Give the extent of all Plasmodium falciparum-infected red blood cells.
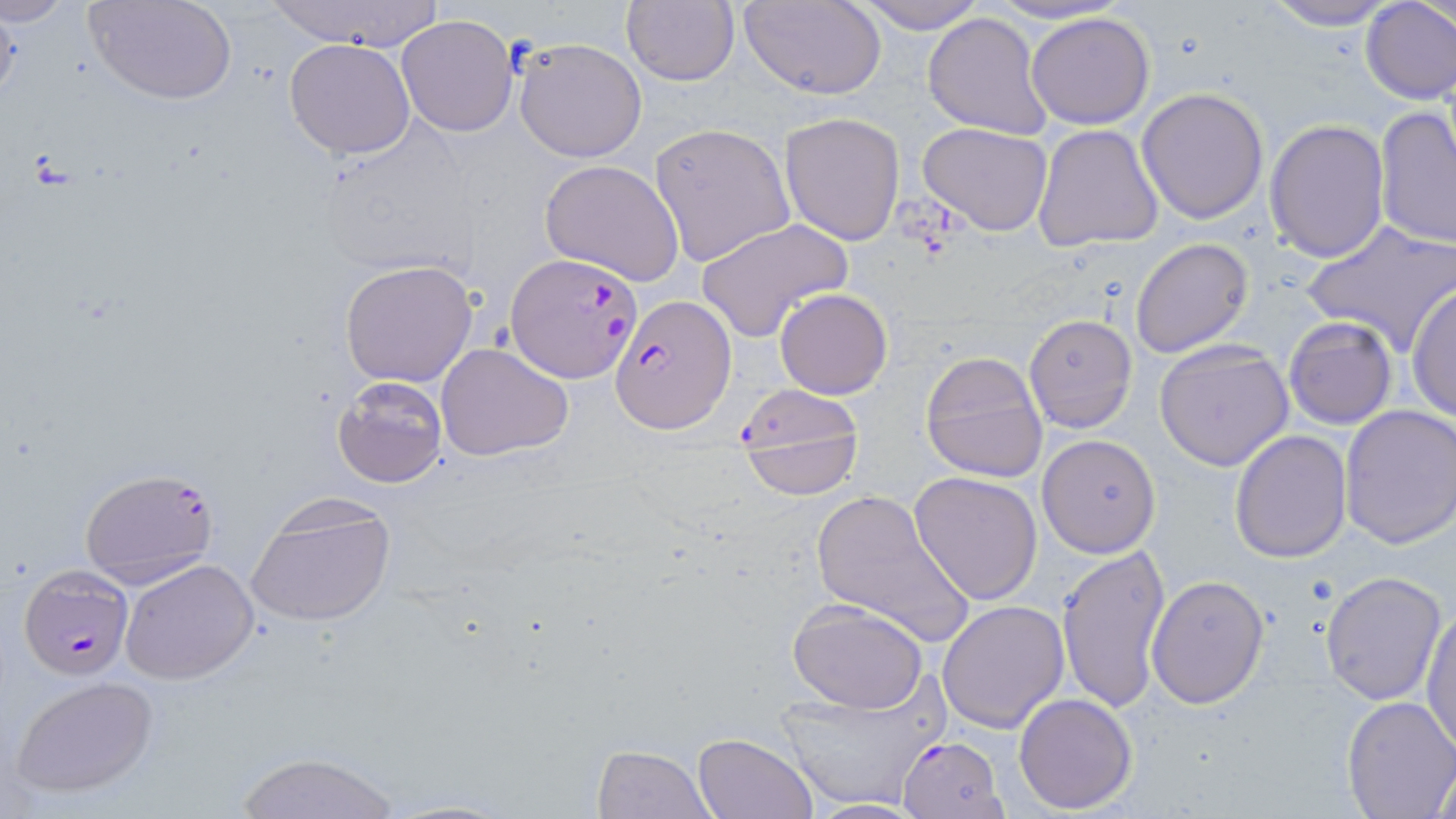

Approximate bounding boxes as [x1, y1, x2, y2] in pixels.
Plasmodium falciparum-infected red blood cells: [506, 254, 642, 382], [610, 292, 736, 434], [733, 383, 863, 489], [78, 467, 219, 589], [16, 566, 133, 680], [895, 734, 1005, 819].

Uninfected red blood cell locations: [91, 0, 237, 106], [265, 0, 446, 52], [740, 0, 887, 100], [850, 0, 985, 34], [984, 0, 1131, 27], [1262, 0, 1402, 30], [1359, 1, 1455, 103], [621, 2, 740, 86], [921, 10, 1055, 141], [1026, 11, 1157, 130], [396, 14, 520, 137], [283, 38, 416, 159], [513, 38, 647, 163], [1136, 88, 1269, 224], [1375, 107, 1456, 250], [778, 111, 907, 247], [1264, 119, 1390, 262], [312, 121, 481, 278], [918, 121, 1054, 237], [648, 122, 795, 267], [1032, 123, 1166, 251], [539, 159, 686, 285], [695, 218, 852, 340], [1302, 221, 1456, 357], [1131, 237, 1253, 357], [336, 259, 480, 387], [1408, 280, 1456, 424], [775, 288, 892, 399], [1023, 314, 1138, 432], [1283, 316, 1398, 431], [1154, 340, 1294, 472], [435, 342, 576, 461], [919, 349, 1049, 481], [331, 375, 448, 488], [1337, 405, 1455, 549], [1229, 429, 1353, 562], [1037, 435, 1160, 558], [909, 472, 1043, 607], [808, 488, 975, 644], [245, 496, 397, 628], [1057, 544, 1171, 713], [120, 557, 258, 684], [1319, 570, 1447, 705], [1146, 575, 1270, 709], [787, 599, 929, 713], [937, 600, 1070, 733], [1423, 602, 1455, 755], [770, 673, 945, 811], [8, 675, 160, 799], [1014, 692, 1139, 814], [1341, 696, 1456, 817], [691, 731, 817, 818], [591, 745, 717, 819], [230, 749, 402, 819], [1428, 753, 1455, 817], [378, 798, 518, 819], [800, 800, 930, 817]. Slide-level diagnosis: Plasmodium falciparum. Single field of view. Image is 1456×819 pixels. May-Grünwald-Giemsa stain. Light microscopy. Captured at 1000x magnification. Thin blood smear.